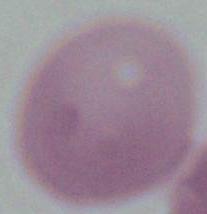
magnification: 1000x
modality: photomicrograph
identification: red blood cell